Locate and identify every blood parasite.
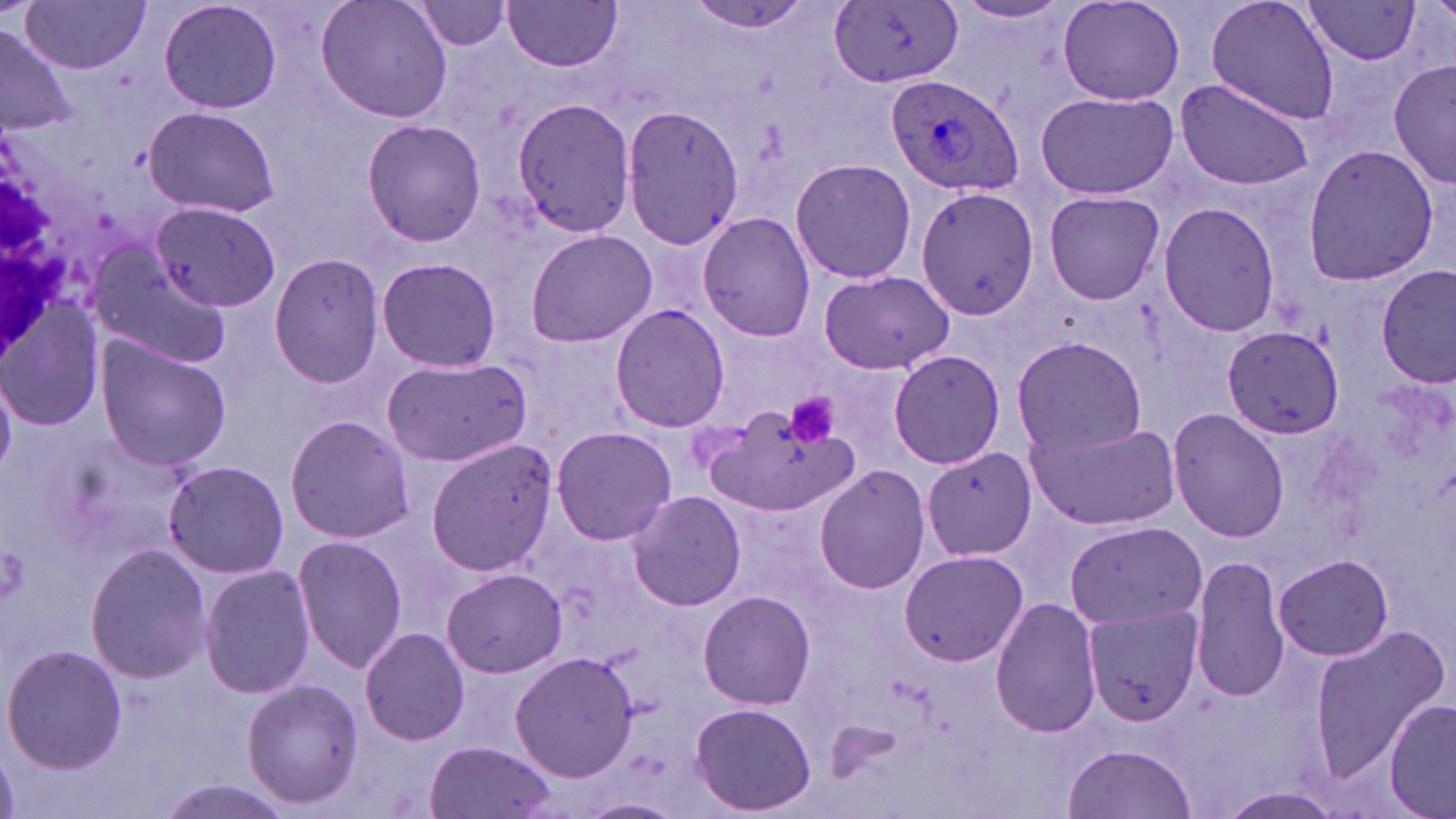

Approximate bounding boxes as (x1,y1)-(x2,y2) corner pairs in pixels.
Plasmodium ovale-infected red blood cells: (885,73)-(1023,198).
No Plasmodium falciparum, Plasmodium malariae, Plasmodium vivax, Babesia divergens, or Trypanosoma brucei observed.

Platelet locations: (783,392)-(842,449). Uninfected red blood cell locations: (157,0)-(284,116), (317,0)-(452,125), (503,0)-(624,72), (1205,0)-(1341,124), (1058,1)-(1185,108), (1304,1)-(1420,65), (19,2)-(151,73), (407,2)-(515,53), (683,2)-(823,35), (831,2)-(962,90), (949,2)-(1074,28), (0,28)-(80,134), (1389,57)-(1455,192), (1176,79)-(1317,193), (1036,91)-(1178,200), (510,95)-(639,238), (143,104)-(279,219), (620,104)-(747,250), (360,118)-(486,247), (1300,142)-(1440,288), (790,158)-(917,284), (915,187)-(1039,320), (1044,190)-(1166,305), (1156,201)-(1281,339), (151,202)-(280,312), (699,209)-(814,343), (524,229)-(658,349), (84,247)-(232,369), (269,253)-(387,389), (377,256)-(501,372), (1377,266)-(1454,387), (819,271)-(954,374), (0,295)-(107,430), (610,304)-(731,433), (1222,327)-(1346,437), (1012,334)-(1146,457), (95,338)-(231,470), (889,348)-(1007,469), (381,358)-(532,465), (704,399)-(857,523), (1167,407)-(1289,542), (284,415)-(414,543), (1023,417)-(1180,528), (550,428)-(677,545), (426,437)-(557,577), (921,447)-(1036,560), (161,460)-(290,578), (813,463)-(931,594), (626,489)-(747,611), (1064,519)-(1207,631), (294,535)-(408,673), (86,542)-(212,684), (900,549)-(1028,667), (1275,553)-(1393,662), (1190,554)-(1289,702), (200,566)-(315,700), (442,568)-(565,677), (698,589)-(815,710), (990,597)-(1103,738), (1085,604)-(1203,727), (1309,625)-(1451,778), (360,628)-(470,745), (2,643)-(126,773), (510,651)-(637,782), (242,678)-(366,809), (1385,701)-(1456,819), (689,702)-(819,814), (424,740)-(559,819), (1064,743)-(1199,819), (153,778)-(299,819), (1220,789)-(1345,818), (574,798)-(686,818). Slide-level diagnosis: Plasmodium ovale. May-Grünwald-Giemsa stain. One field of a larger specimen. Thin blood film. 1000x magnification. Image is 1456×819 pixels. Optical microscopy.